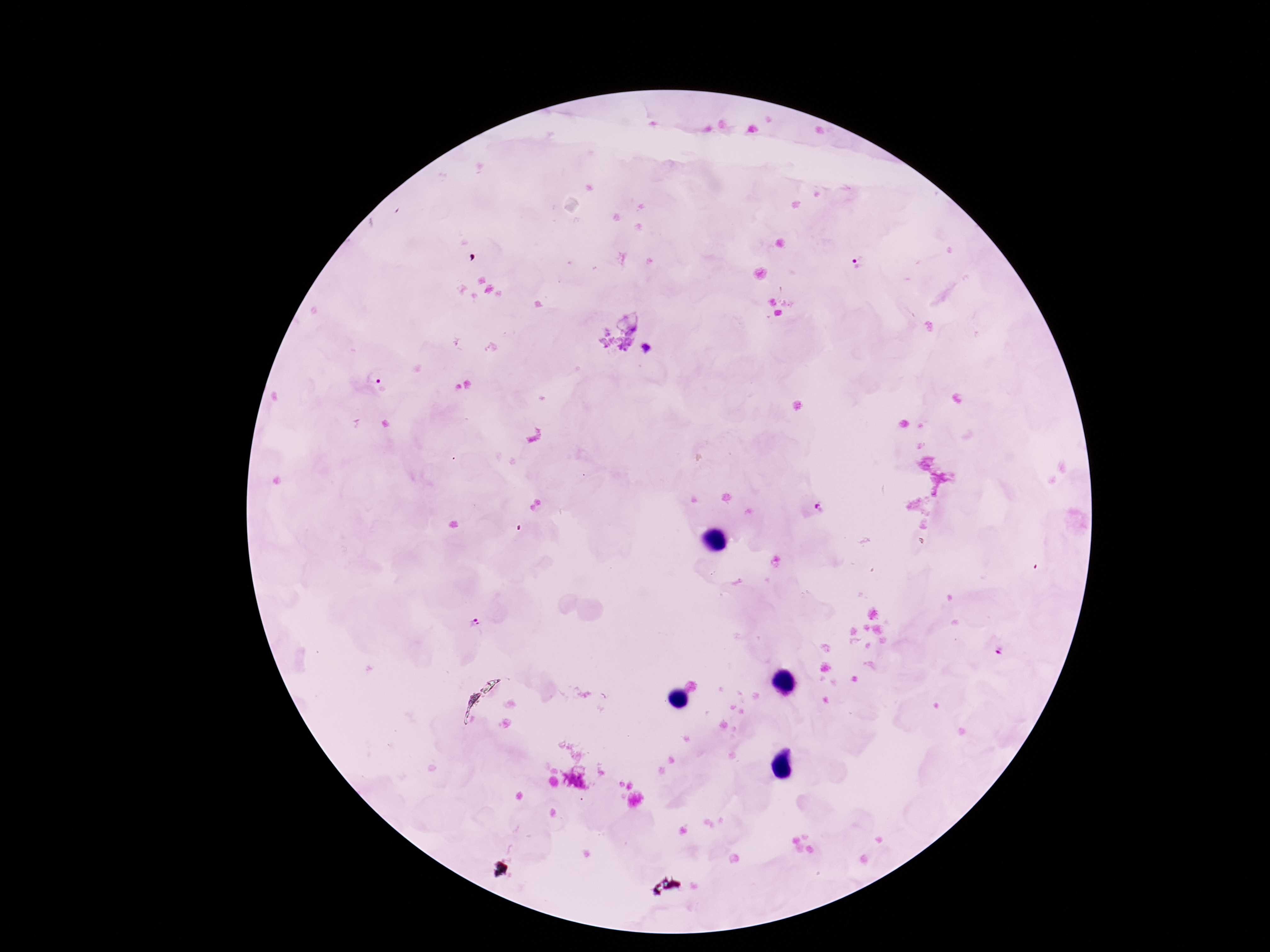
preparation = thick peripheral-blood smear
stain = Giemsa
field of view = one from this slide
patient malaria status = infected
magnification = 100x
capture = smartphone camera through the microscope eyepiece
Plasmodium parasite locations = approximate centers as {x, y} in pixels: {861, 260}, {375, 375}, {820, 507}, {474, 623}, {1000, 649}
image size = 1270×952 pixels